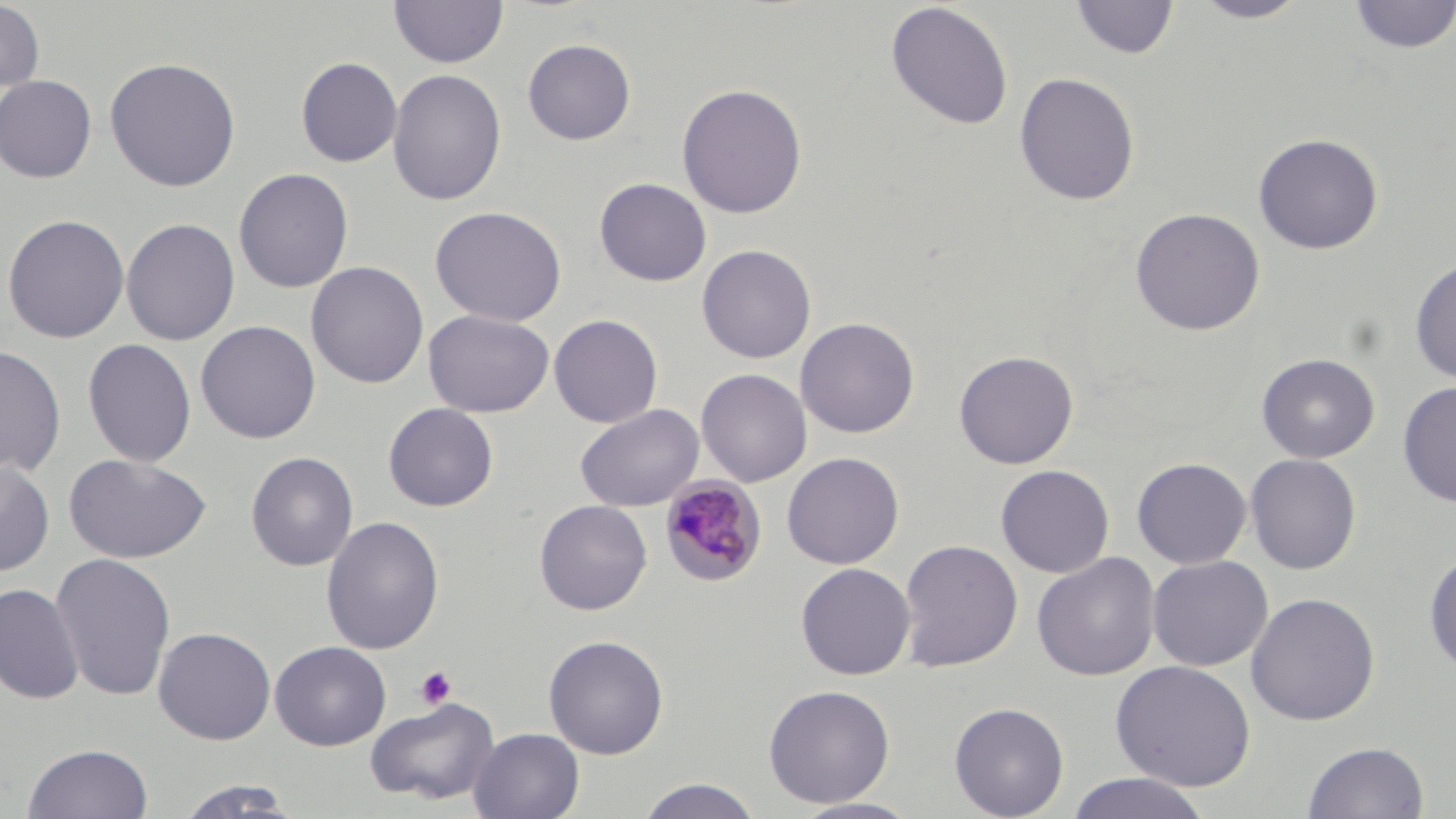

Approximate bounding boxes as named x1/y1/x2/y2 corners in pixels. Platelet locations: (x1=415, y1=665, x2=457, y2=710). Uninfected red blood cell locations: (x1=0, y1=0, x2=44, y2=93), (x1=389, y1=0, x2=508, y2=68), (x1=1071, y1=0, x2=1179, y2=60), (x1=1192, y1=0, x2=1311, y2=23), (x1=1348, y1=0, x2=1456, y2=53), (x1=885, y1=2, x2=1014, y2=130), (x1=522, y1=39, x2=636, y2=145), (x1=296, y1=56, x2=403, y2=167), (x1=104, y1=57, x2=241, y2=192), (x1=387, y1=69, x2=507, y2=206), (x1=1014, y1=72, x2=1140, y2=206), (x1=0, y1=75, x2=97, y2=183), (x1=675, y1=83, x2=808, y2=219), (x1=1253, y1=133, x2=1384, y2=255), (x1=233, y1=168, x2=354, y2=293), (x1=594, y1=178, x2=712, y2=286), (x1=430, y1=206, x2=567, y2=327), (x1=1130, y1=207, x2=1265, y2=336), (x1=2, y1=214, x2=130, y2=343), (x1=121, y1=218, x2=240, y2=345), (x1=697, y1=244, x2=817, y2=364), (x1=1410, y1=255, x2=1456, y2=384), (x1=306, y1=261, x2=429, y2=388), (x1=423, y1=309, x2=554, y2=417), (x1=549, y1=314, x2=663, y2=428), (x1=795, y1=317, x2=920, y2=438), (x1=196, y1=320, x2=321, y2=443), (x1=83, y1=338, x2=197, y2=467), (x1=0, y1=345, x2=66, y2=477), (x1=953, y1=350, x2=1079, y2=469), (x1=1256, y1=353, x2=1379, y2=463), (x1=696, y1=368, x2=812, y2=487), (x1=1397, y1=381, x2=1456, y2=508), (x1=383, y1=403, x2=499, y2=511), (x1=575, y1=403, x2=703, y2=511), (x1=245, y1=451, x2=358, y2=571), (x1=782, y1=452, x2=904, y2=569), (x1=63, y1=453, x2=212, y2=564), (x1=1245, y1=453, x2=1362, y2=574), (x1=1131, y1=457, x2=1251, y2=569), (x1=0, y1=458, x2=56, y2=576), (x1=995, y1=464, x2=1114, y2=578), (x1=534, y1=499, x2=652, y2=615), (x1=320, y1=516, x2=445, y2=655), (x1=898, y1=539, x2=1023, y2=672), (x1=1423, y1=548, x2=1456, y2=679), (x1=50, y1=553, x2=177, y2=702), (x1=1031, y1=553, x2=1160, y2=681), (x1=1147, y1=555, x2=1273, y2=671), (x1=795, y1=562, x2=916, y2=680), (x1=0, y1=583, x2=85, y2=705), (x1=1245, y1=592, x2=1380, y2=726), (x1=153, y1=626, x2=276, y2=744), (x1=543, y1=634, x2=669, y2=759), (x1=270, y1=641, x2=391, y2=751), (x1=1110, y1=660, x2=1257, y2=793), (x1=763, y1=684, x2=895, y2=808), (x1=364, y1=696, x2=500, y2=806), (x1=949, y1=702, x2=1069, y2=818), (x1=469, y1=727, x2=585, y2=819), (x1=1302, y1=741, x2=1429, y2=819), (x1=22, y1=742, x2=154, y2=819), (x1=1065, y1=772, x2=1214, y2=819), (x1=635, y1=778, x2=765, y2=818), (x1=172, y1=781, x2=304, y2=818), (x1=788, y1=798, x2=924, y2=818). Plasmodium malariae-infected red blood cell locations: (x1=659, y1=475, x2=768, y2=587). Slide-level diagnosis: Plasmodium malariae. Thin blood film. Image is 1456×819 pixels. Captured at 1000x magnification. One field of a larger specimen. May-Grünwald-Giemsa stain. Optical microscopy.